Point out each malaria parasite.
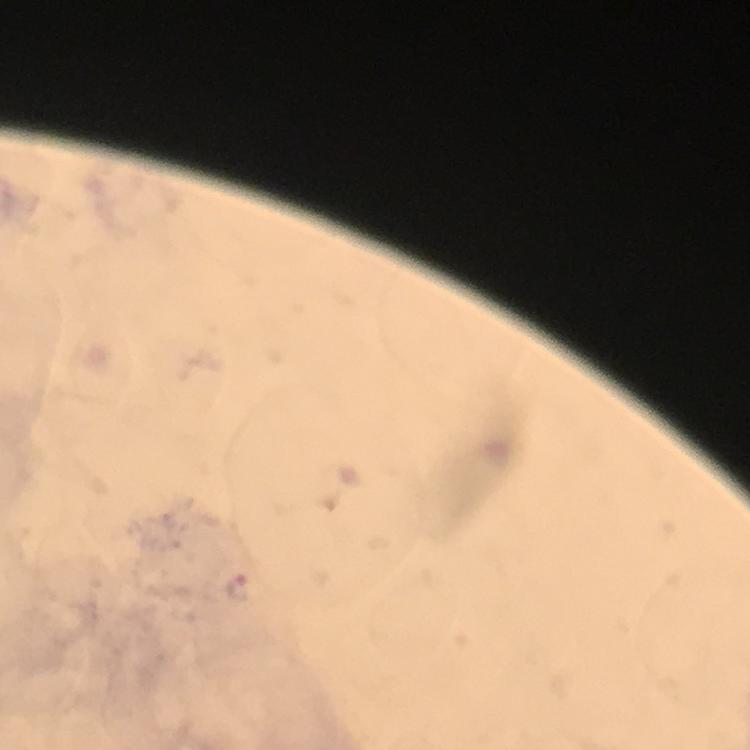
Approximate centers as [x, y] in pixels.
Malaria parasites: [239, 587].

{
  "immersion_oil": "used",
  "image_size": "750×750 pixels",
  "cropped_from": "one field of view",
  "context": "from a diagnostic examination for malaria",
  "preparation": "thick blood film",
  "stain": "Giemsa",
  "magnification": "100x",
  "capture": "smartphone photograph through a microscope"
}